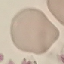

Summary:
  - Result: negative for malaria parasites
  - Capture: smartphone through the microscope eyepiece
  - Preparation: thin blood smear
  - Image type: cell patch, automatically extracted from a larger field of view and resized to 64 × 64 pixels
  - Stain: Giemsa